Report the malaria status of this cell.
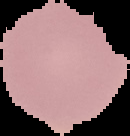
Uninfected.

The area outside the segmented cell region is set to black. From a thin blood smear. Image is 130×136 pixels.